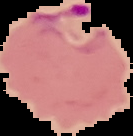
Summary:
  - Image type: segmented cell region with the area outside set to black
  - Preparation: thin blood smear
  - Result: Plasmodium parasites identified
  - Image size: 133×136 pixels